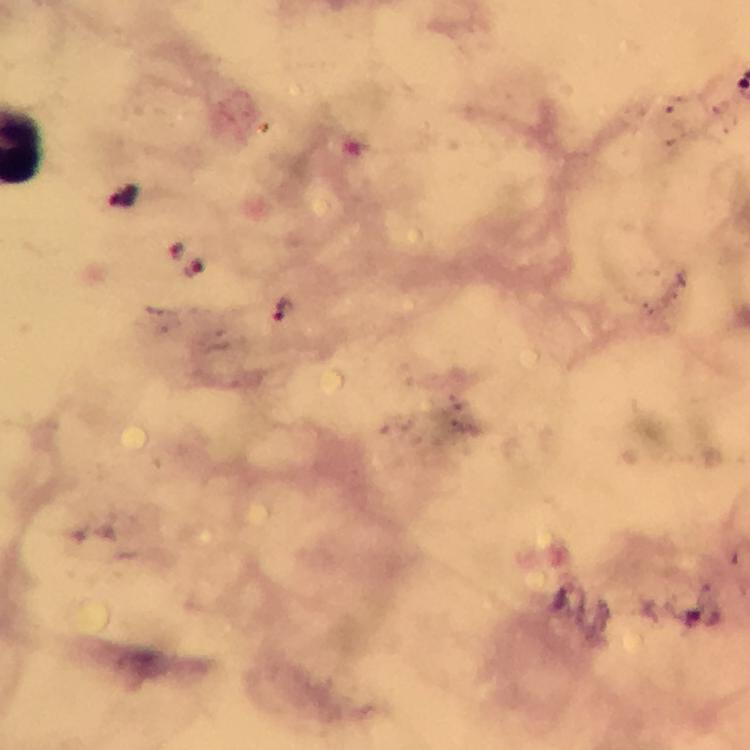 Approximate centers as {x, y} in pixels. Plasmodium parasite locations: {196, 269}, {282, 311}. Immersion oil was used. Image is 750×750 pixels. Giemsa stain. 100x magnification. Cropped region of a single field of view. From a malaria diagnostic workup. Thick blood film. Smartphone photograph taken through a microscope.